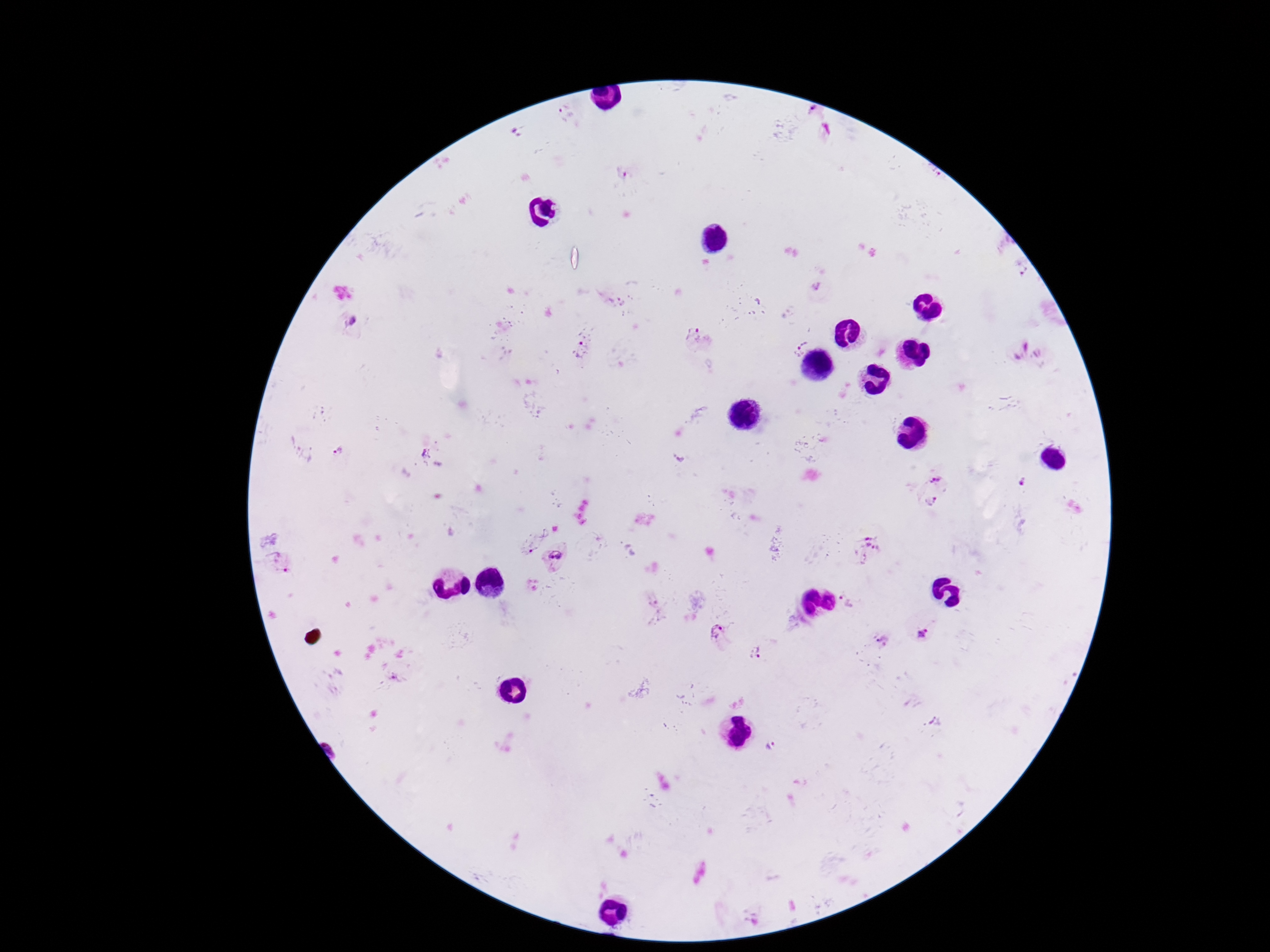
Approximate object centers, in pixels from the top-left corner.
Summary:
  - Plasmodium parasite locations: (x=563, y=105), (x=812, y=109), (x=622, y=173), (x=933, y=174), (x=1023, y=269), (x=816, y=287), (x=352, y=322), (x=692, y=332), (x=798, y=343), (x=1018, y=349), (x=580, y=350), (x=337, y=449), (x=424, y=451), (x=935, y=476), (x=1023, y=483), (x=932, y=501), (x=530, y=544), (x=867, y=549), (x=555, y=555), (x=289, y=563), (x=848, y=602), (x=717, y=632), (x=922, y=633), (x=880, y=640), (x=757, y=653), (x=772, y=746)
  - Patient malaria status: infected
  - Magnification: 100x
  - Stain: Giemsa
  - Capture: smartphone camera through the microscope eyepiece
  - Field of view: single
  - Preparation: thick blood smear
  - Image size: 1270×952 pixels